Assess the morphology of the red blood cells.
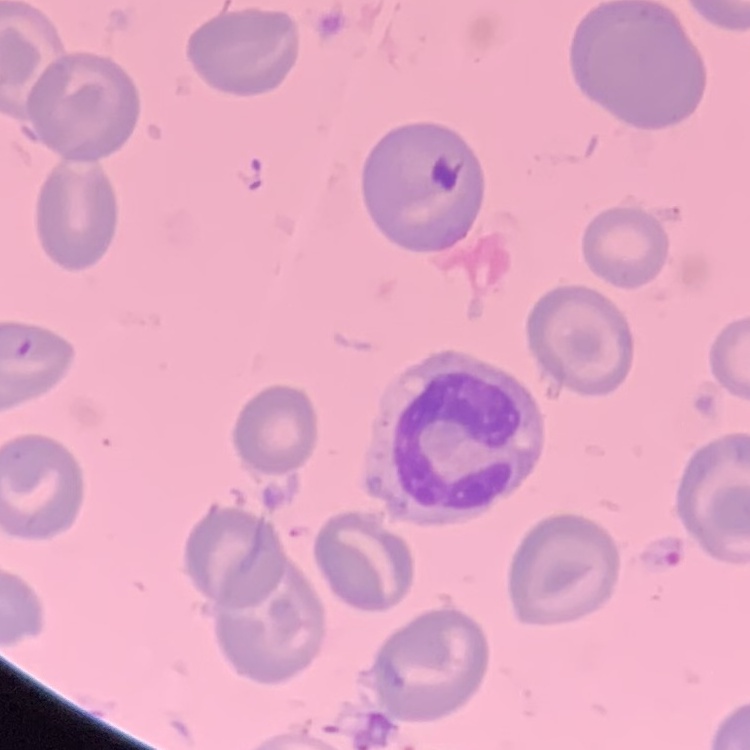
They show no rouleaux formation.

Summary:
  - Image type: one tile cut from a larger photomicrograph
  - Stain: Field's or Giemsa
  - Preparation: thin blood film